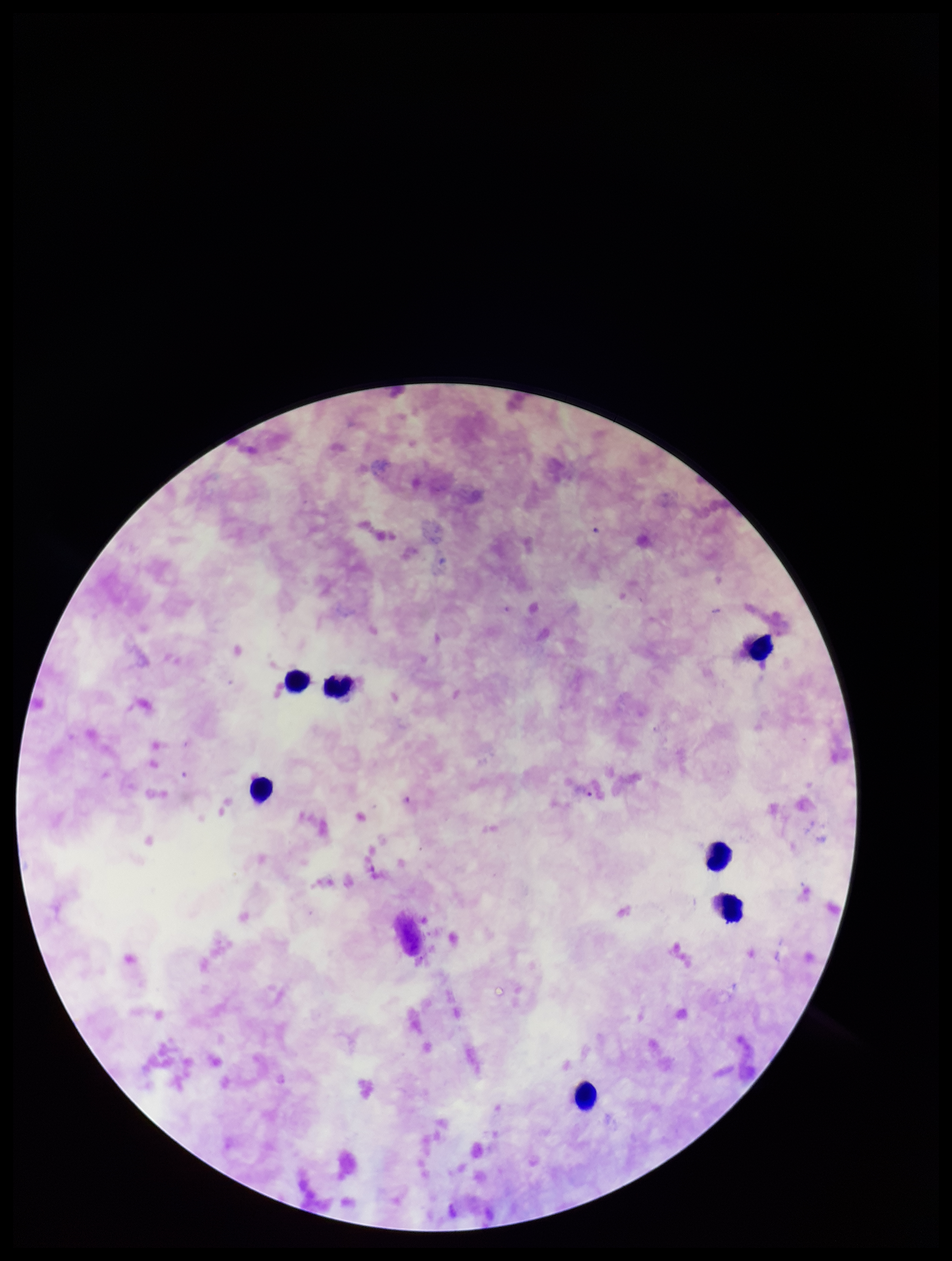
Summary:
  - Parasite count: 0
  - Preparation: thick
  - Stain: Giemsa
  - Leukocyte count: 7
  - Image size: 952×1261 pixels
  - Capture: smartphone photograph through the microscope eyepiece
  - Species reported for this patient: Plasmodium falciparum
  - Plasmodium parasites: none seen
  - Field of view: single
  - Patient malaria status: infected